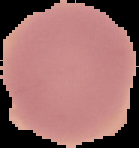 Result: negative for malaria parasites. Image is 139×148 pixels. The area outside the segmented cell region is set to black. From a thin blood smear.